State the blood parasite species.
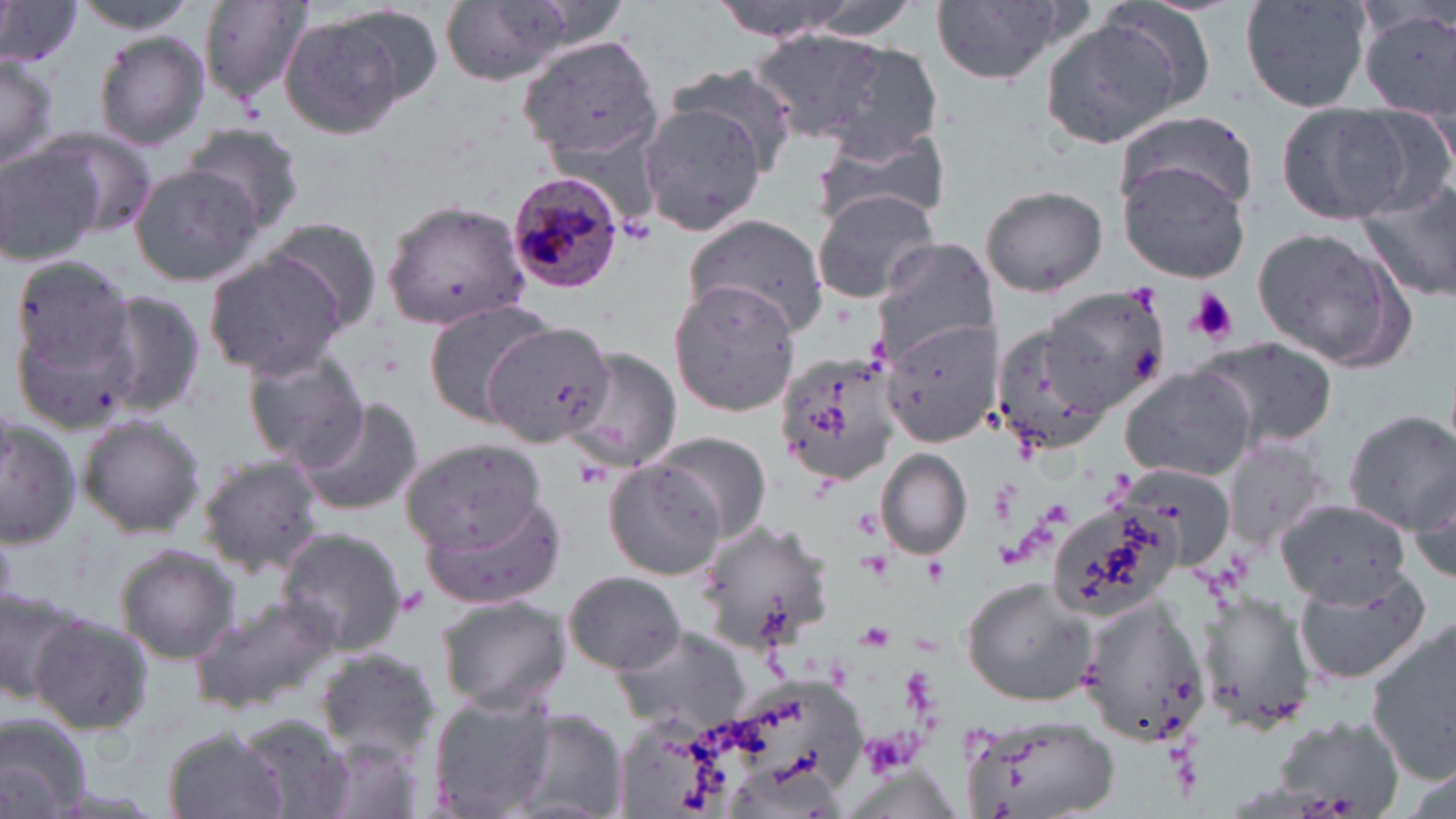
Plasmodium malariae.

uninfected red blood cell locations = approximate bounding boxes as (x1, y1, x2, y2) in pixels: (69, 0, 203, 32), (196, 0, 312, 102), (435, 0, 583, 86), (703, 0, 873, 40), (928, 0, 1081, 88), (0, 1, 82, 69), (1241, 1, 1372, 116), (278, 10, 415, 138), (1362, 10, 1456, 119), (1038, 15, 1196, 150), (751, 30, 905, 144), (92, 31, 211, 150), (515, 33, 664, 165), (0, 54, 60, 171), (663, 62, 801, 173), (639, 102, 770, 237), (1278, 103, 1428, 223), (1112, 111, 1259, 219), (182, 124, 305, 237), (811, 124, 949, 230), (36, 127, 157, 240), (0, 142, 102, 267), (1119, 159, 1250, 281), (128, 164, 263, 285), (1356, 174, 1456, 305), (982, 183, 1109, 298), (810, 188, 942, 305), (382, 199, 530, 330), (682, 214, 829, 338), (262, 215, 387, 330), (1249, 225, 1413, 373), (870, 237, 996, 363), (202, 251, 349, 378), (10, 255, 137, 386), (667, 280, 802, 418), (1044, 285, 1170, 413), (95, 287, 211, 419), (423, 298, 553, 424), (482, 317, 618, 447), (880, 318, 998, 445), (992, 320, 1117, 459), (1197, 337, 1337, 453), (563, 348, 682, 471), (774, 348, 898, 483), (243, 349, 369, 468), (1121, 367, 1256, 481), (290, 395, 425, 516), (1341, 409, 1456, 535), (76, 415, 205, 537), (1, 417, 83, 549), (649, 432, 772, 542), (1223, 437, 1330, 550), (400, 439, 551, 556), (877, 449, 972, 559), (196, 453, 325, 575), (603, 456, 725, 580), (1111, 462, 1241, 570), (1410, 469, 1456, 588), (422, 492, 566, 610), (1274, 501, 1414, 605), (1047, 504, 1179, 620), (696, 518, 838, 656), (276, 528, 407, 654), (114, 545, 241, 663), (1292, 569, 1432, 684), (563, 570, 684, 673), (962, 576, 1096, 706), (0, 583, 84, 704), (1200, 592, 1314, 732), (1069, 593, 1210, 748), (435, 594, 569, 714), (186, 595, 342, 715), (28, 613, 153, 736), (1365, 618, 1456, 782), (610, 625, 752, 733), (315, 649, 441, 757), (427, 692, 558, 818), (957, 709, 1120, 819), (505, 711, 627, 819), (0, 714, 92, 819), (234, 714, 357, 818), (1270, 715, 1410, 815), (164, 730, 290, 819), (1398, 766, 1454, 816)
Plasmodium malariae-infected red blood cell locations = approximate bounding boxes as (x1, y1, x2, y2) in pixels: (505, 171, 624, 295)
modality = optical microscopy
magnification = 1000x
image size = 1456×819 pixels
preparation = thin blood film
platelet locations = approximate bounding boxes as (x1, y1, x2, y2) in pixels: (1186, 289, 1238, 345)
field of view = single
stain = May-Grünwald-Giemsa